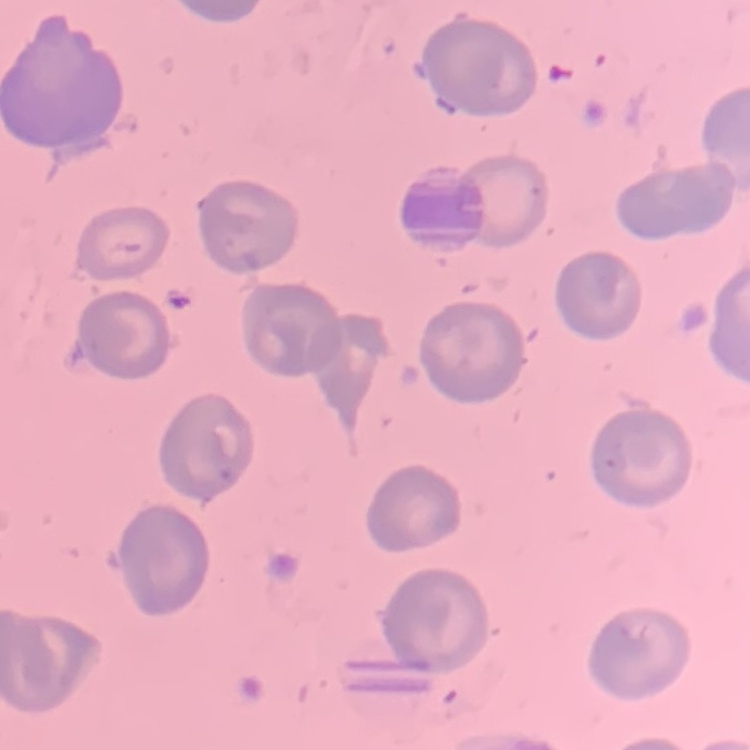
erythrocyte_morphology: no rouleaux formation
image_type: one tile cut from a larger photomicrograph
stain: Field's or Giemsa
preparation: thin blood film